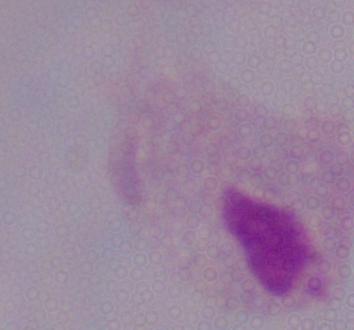

Photomicrograph. 1000x magnification. A trichomonad is seen.